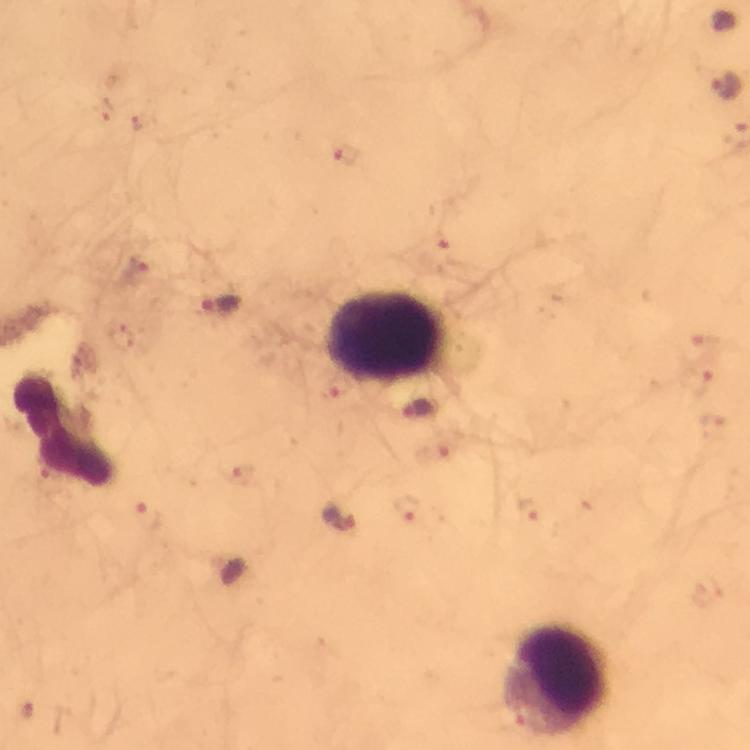

Approximate centers as [x, y] in pixels. Plasmodium parasite locations: [726, 88], [346, 152], [438, 243], [137, 270], [222, 302], [705, 344], [700, 382], [338, 387], [436, 452], [242, 478], [409, 509], [531, 510], [149, 515], [342, 517]. Leukocyte locations: [389, 339], [65, 427], [556, 677]. Photographed through the microscope with a smartphone camera. Immersion oil applied. At 100x magnification. Giemsa stain. From a diagnostic examination for malaria. Thick smear. Cropped region of a single field of view. Image is 750×750 pixels.